Report the malaria status of this cell.
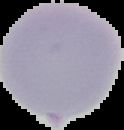

Uninfected.

Image is 124×130 pixels. From a thin blood film. Segmented cell region on a black background.